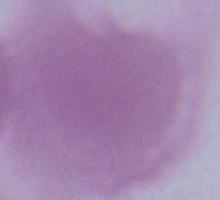

Summary:
  - Identification: erythrocyte
  - Modality: micrograph
  - Magnification: 1000x